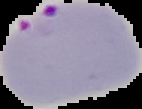 Result: Plasmodium parasites identified. From a thin blood smear. Image is 142×109 pixels. The area outside the segmented cell region is set to black.